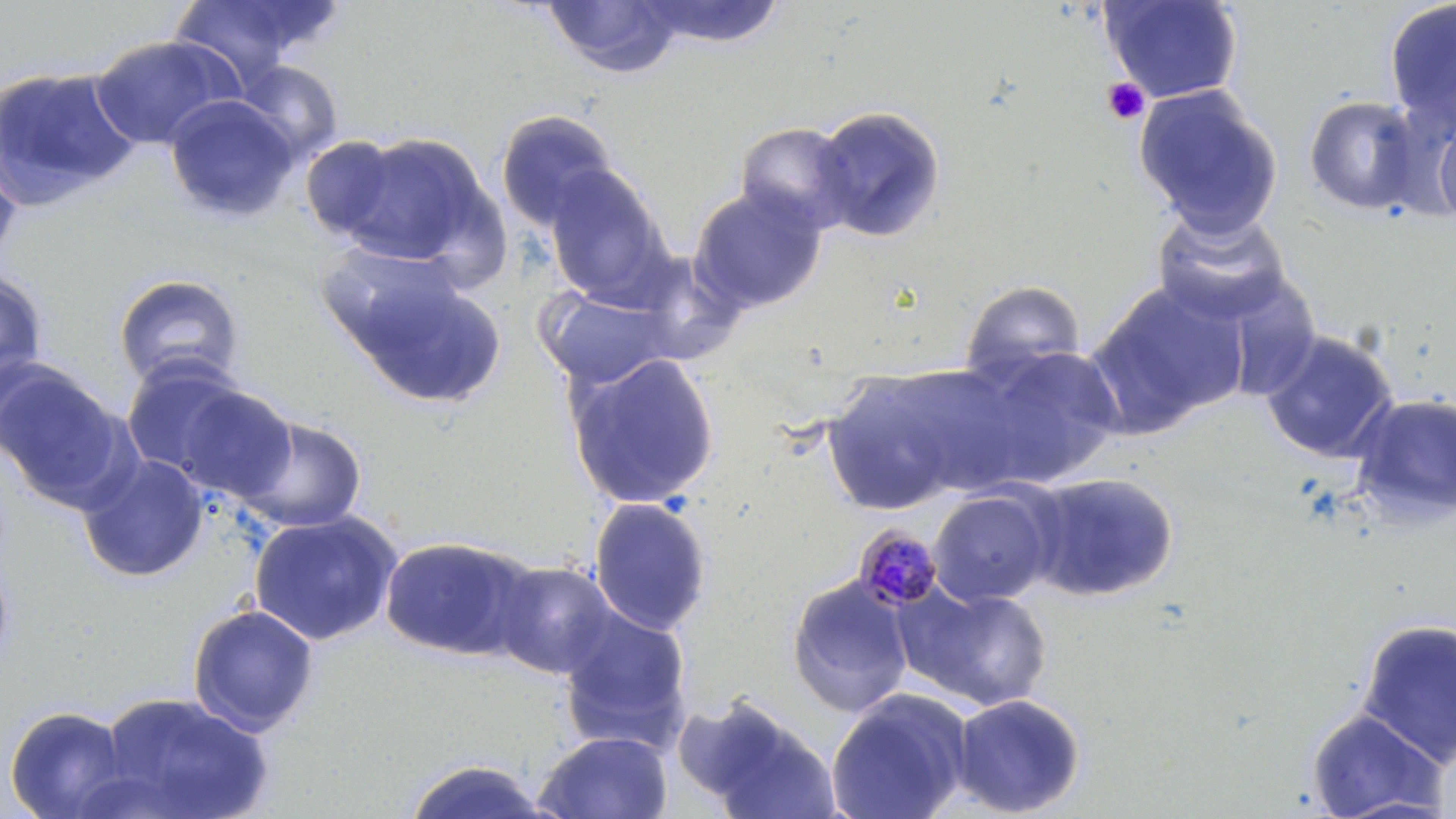

{
  "slide_level_diagnosis": "Plasmodium malariae",
  "image_size": "1456×819 pixels",
  "magnification": "1000x",
  "stain": "May-Grünwald-Giemsa",
  "modality": "light microscopy",
  "field_of_view": "single",
  "uninfected_red_blood_cell_locations": "approximate bounding boxes as (x1, y1, x2, y2) in pixels: (167, 0, 336, 87), (542, 0, 685, 78), (635, 0, 788, 48), (1098, 0, 1244, 103), (1383, 1, 1456, 134), (89, 34, 241, 150), (234, 60, 344, 163), (0, 65, 140, 210), (1133, 84, 1283, 238), (164, 94, 300, 221), (1303, 94, 1425, 216), (810, 105, 947, 244), (495, 110, 619, 231), (1432, 113, 1456, 228), (733, 121, 858, 234), (332, 131, 498, 272), (299, 136, 403, 241), (0, 147, 23, 269), (544, 165, 670, 303), (688, 185, 828, 315), (1150, 206, 1293, 326), (314, 242, 474, 367), (626, 249, 747, 366), (349, 269, 507, 409), (0, 271, 49, 401), (1197, 273, 1324, 405), (113, 274, 244, 390), (959, 279, 1087, 389), (1086, 281, 1248, 435), (540, 288, 678, 389), (1260, 330, 1400, 464), (963, 343, 1125, 489), (566, 352, 721, 510), (118, 358, 266, 489), (0, 359, 131, 511), (821, 366, 976, 515), (163, 380, 298, 507), (1350, 393, 1456, 527), (229, 413, 368, 535), (77, 453, 210, 583), (1024, 470, 1180, 602), (928, 488, 1056, 607), (589, 496, 713, 635), (248, 510, 402, 646), (379, 535, 537, 662), (490, 560, 619, 679), (786, 576, 913, 717), (895, 582, 1055, 712), (186, 603, 320, 736), (557, 608, 693, 751), (1355, 618, 1455, 768), (825, 688, 973, 819), (95, 691, 272, 819), (951, 693, 1085, 817), (678, 697, 838, 817), (2, 704, 134, 819), (1304, 709, 1448, 817), (533, 730, 674, 819), (401, 758, 556, 818)",
  "preparation": "thin blood smear",
  "platelet_locations": "approximate bounding boxes as (x1, y1, x2, y2) in pixels: (1101, 77, 1151, 126)",
  "plasmodium_malariae_infected_red_blood_cell_locations": "approximate bounding boxes as (x1, y1, x2, y2) in pixels: (852, 523, 945, 612)"
}